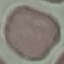

Summary:
  - Malaria status: uninfected
  - Stain: Giemsa
  - Preparation: thin blood smear
  - Image type: cell patch, automatically extracted from a larger field of view and resized to 64 × 64 pixels
  - Capture: smartphone camera at the microscope eyepiece